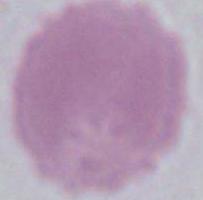
Summary:
  - Identification: red blood cell
  - Magnification: 1000x
  - Modality: micrograph